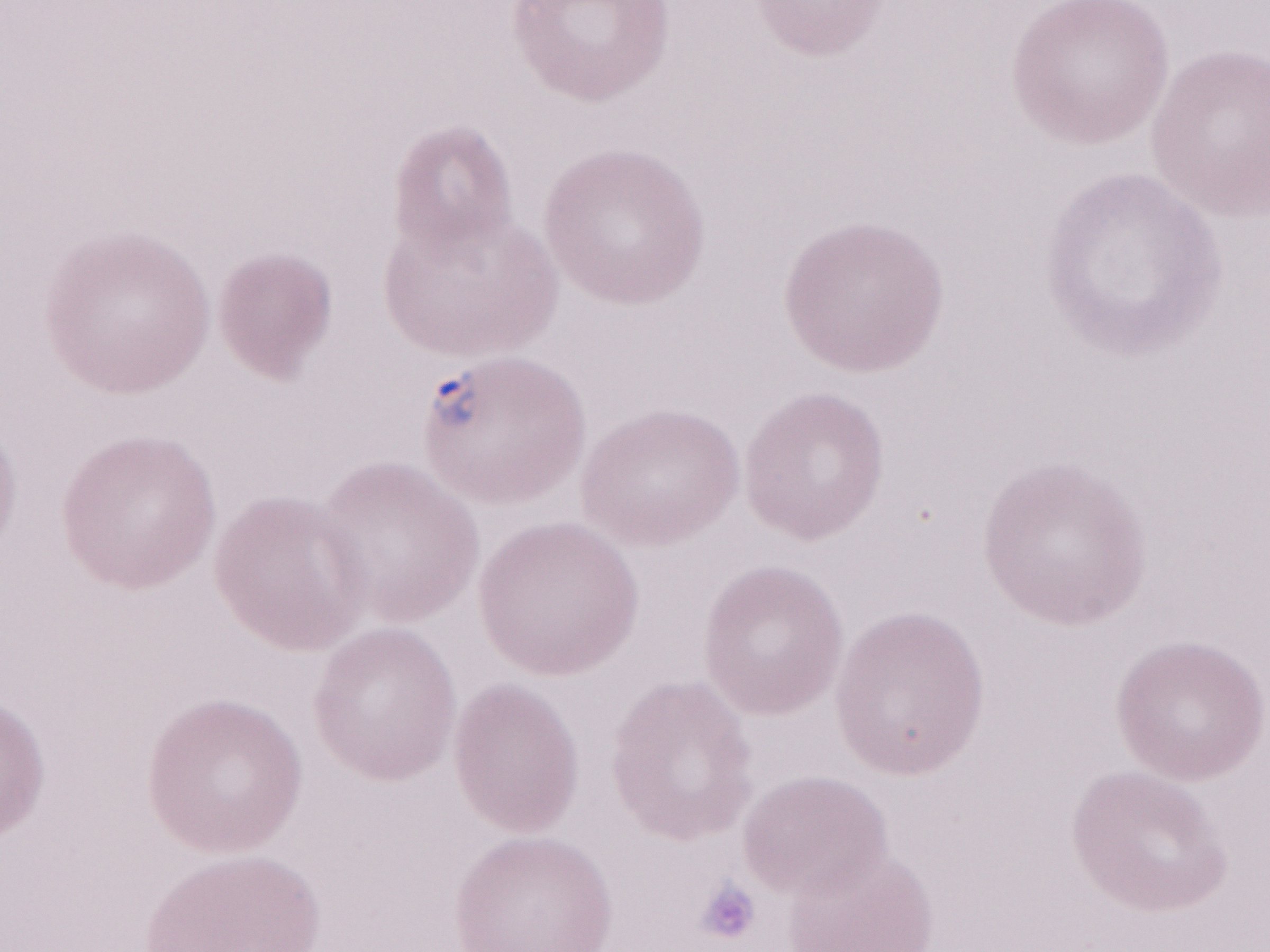
Thin blood smear. Patient-level malaria diagnosis: positive. Single field of view. May-Grünwald-Giemsa (MGG) stain. 1,000x magnification. Olympus BX43 microscope and DP73 digital camera. Image is 1270×952 pixels.